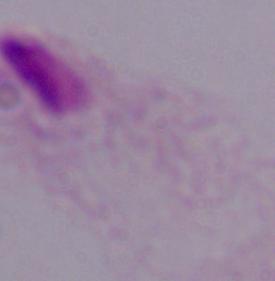

Summary:
  - Modality: photomicrograph
  - Identification: trichomonad
  - Magnification: 1000x